Locate every leukocyte (white blood cell).
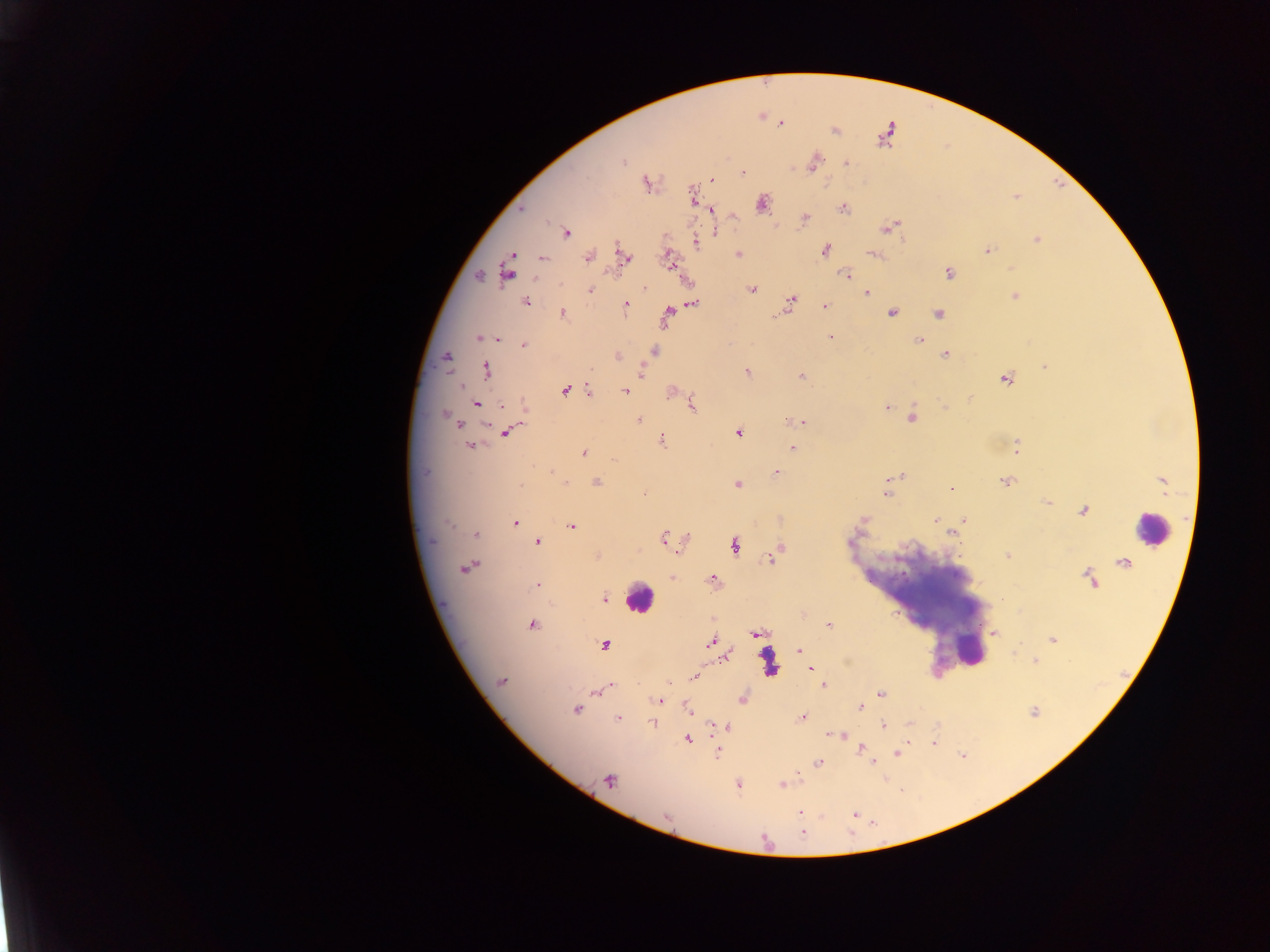

Approximate centers as [x, y] in pixels.
Leukocytes: [1149, 528], [638, 598], [968, 647].

Plasmodium parasite locations: [781, 124], [835, 130], [816, 159], [622, 160], [847, 163], [814, 165], [744, 174], [711, 180], [645, 183], [692, 195], [1016, 197], [761, 203], [843, 209], [711, 211], [733, 215], [805, 217], [888, 228], [566, 233], [716, 233], [1036, 239], [696, 244], [825, 250], [988, 250], [738, 254], [872, 254], [513, 255], [623, 255], [588, 257], [542, 259], [669, 262], [1012, 268], [948, 273], [508, 274], [847, 274], [480, 276], [590, 290], [752, 290], [866, 292], [1014, 296], [790, 301], [525, 302], [626, 304], [694, 304], [825, 306], [893, 312], [563, 313], [668, 313], [938, 314], [831, 337], [479, 338], [497, 338], [919, 340], [523, 345], [654, 351], [945, 354], [447, 357], [617, 357], [1044, 366], [487, 369], [747, 372], [641, 373], [801, 376], [1005, 379], [462, 386], [566, 390], [588, 390], [625, 391], [672, 391], [970, 398], [692, 404], [477, 405], [502, 405], [945, 407], [887, 408], [446, 415], [912, 418], [638, 419], [802, 422], [458, 424], [506, 433], [738, 434], [663, 441], [471, 446], [792, 447], [1017, 448], [583, 453], [613, 460], [552, 473], [776, 473], [898, 476], [1005, 481], [596, 482], [1162, 482], [564, 483], [738, 484], [520, 485], [951, 489], [886, 493], [644, 494], [1047, 502], [1083, 511], [964, 519], [935, 521], [515, 523], [449, 524], [571, 526], [476, 534], [952, 534], [663, 537], [538, 542], [734, 546], [780, 548], [1007, 556], [771, 557], [466, 568], [671, 577], [713, 579], [1090, 579], [538, 585], [604, 599], [532, 625], [828, 625], [994, 633], [757, 634], [1052, 640], [710, 643], [604, 644], [799, 650], [726, 655], [1035, 661], [811, 668], [694, 677], [501, 681], [669, 683], [611, 685], [824, 686], [597, 692], [880, 694], [743, 699], [659, 700], [860, 706], [576, 710], [688, 710], [804, 717], [617, 718], [653, 723], [884, 725], [711, 726], [727, 726], [842, 735], [833, 736], [688, 739], [934, 743], [861, 748], [717, 753], [897, 754], [873, 762], [818, 763], [608, 781], [738, 784], [781, 785], [799, 811], [855, 814], [666, 816], [802, 826], [803, 832]. One field of view. Thick blood film. Image is 1270×952 pixels. Mobile-phone photograph taken through the microscope. Collected in Ghana.